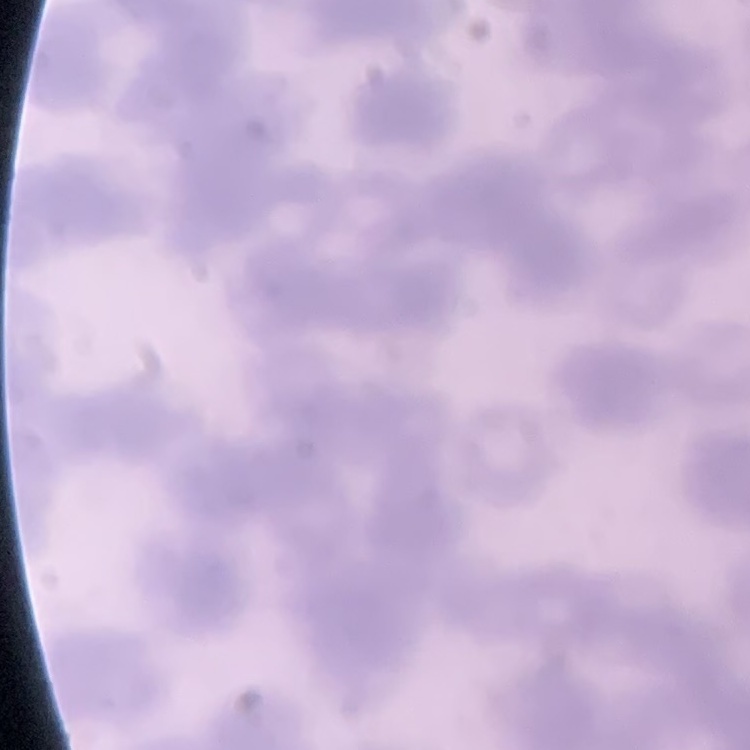
The erythrocytes exhibit rouleaux formation. Square crop of a larger photomicrograph. Thin blood smear. Field's or Giemsa stain.